Comment on the morphology of the red blood cells.
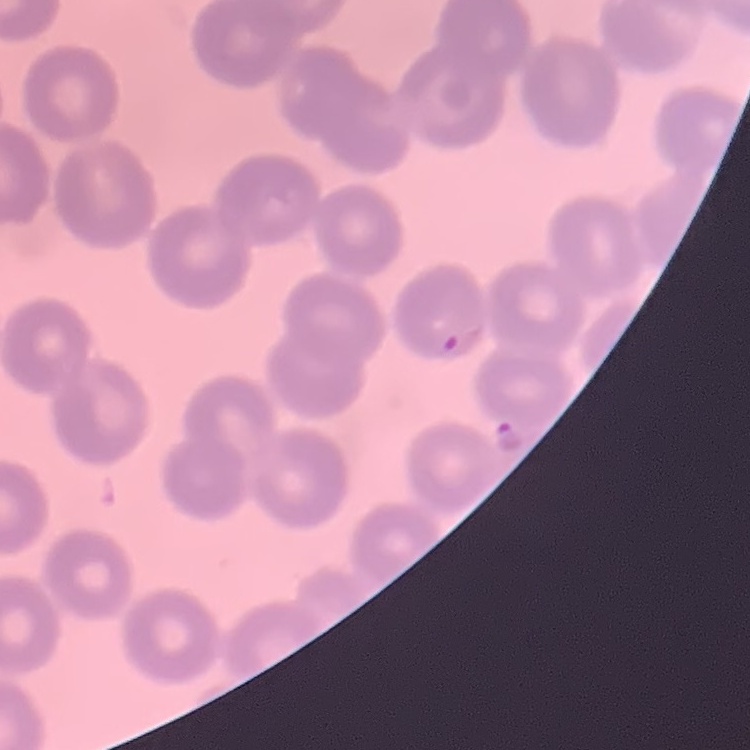
They show no rouleaux formation.

Summary:
  - Preparation: thin blood film
  - Image type: one tile cut from a larger photomicrograph
  - Stain: Field's or Giemsa